Comment on the morphology of the erythrocytes.
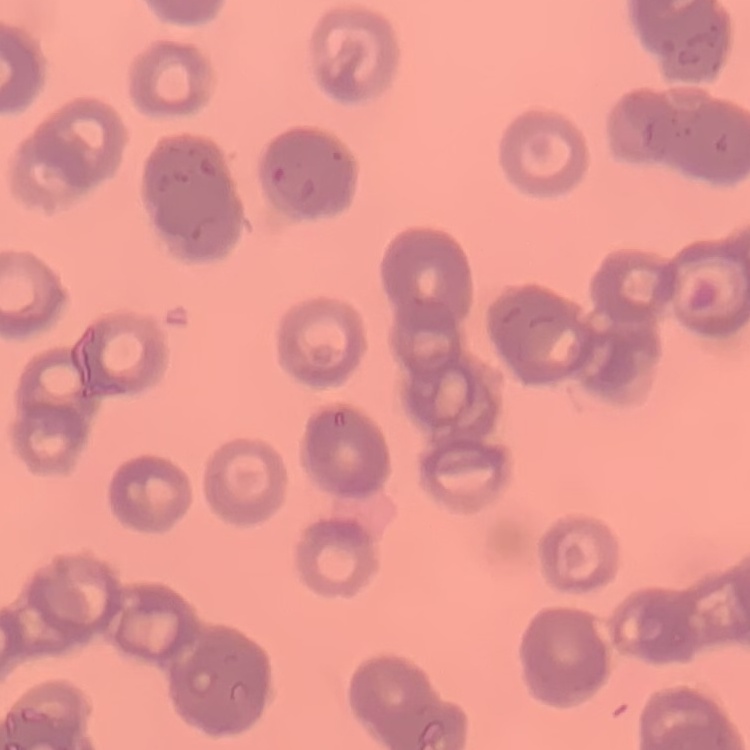

Rouleaux formation.

image type = square crop of a larger photomicrograph
stain = Field's or Giemsa
preparation = thin blood film